State the preparation type.
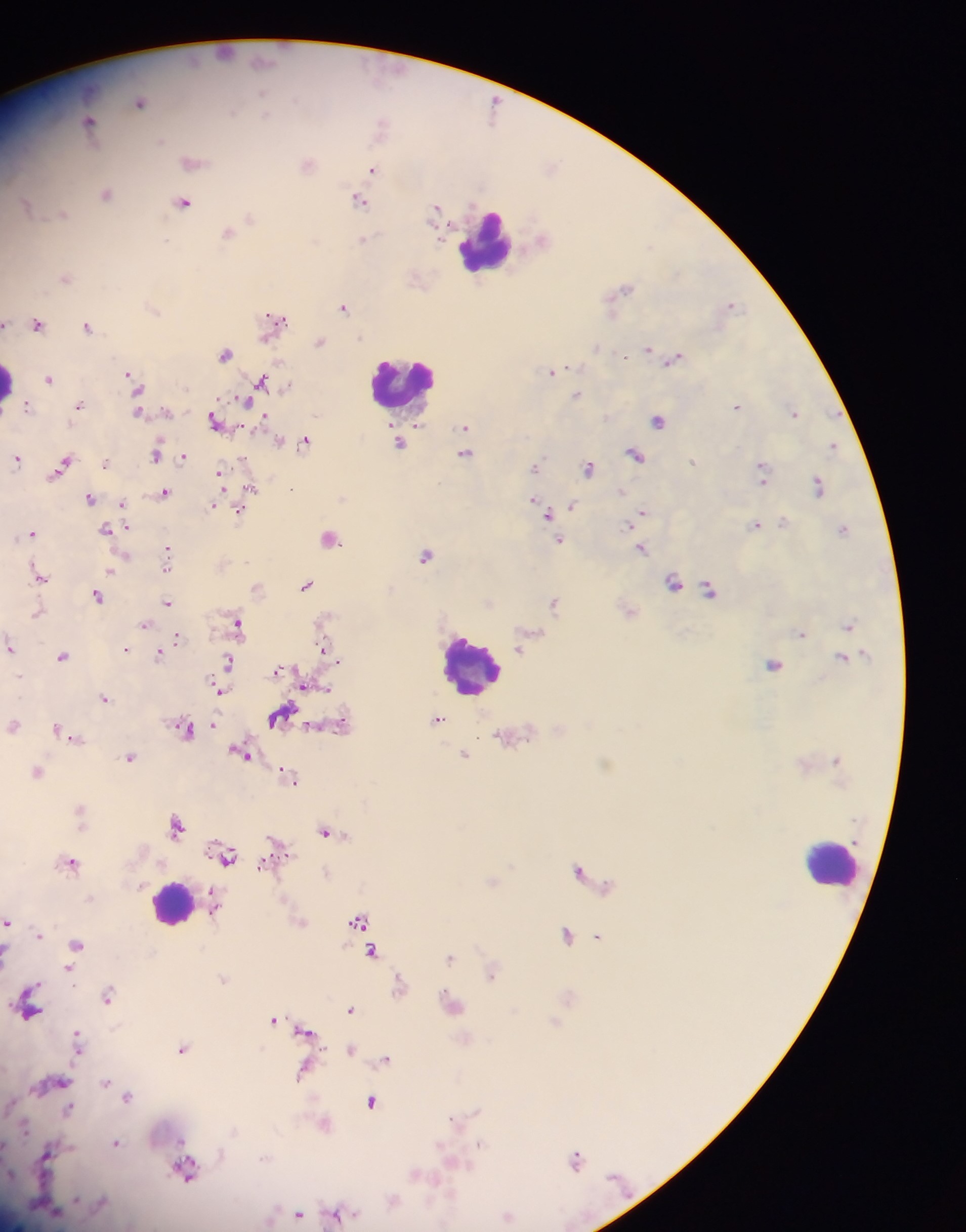

Thick blood film.

Approximate centers as {x, y} in pixels. Malaria parasite locations: {225, 52}, {141, 102}, {494, 107}, {90, 122}, {383, 125}, {192, 161}, {309, 163}, {373, 169}, {107, 192}, {359, 199}, {184, 201}, {27, 206}, {436, 209}, {62, 214}, {250, 218}, {229, 231}, {363, 240}, {66, 276}, {418, 278}, {625, 288}, {732, 303}, {344, 306}, {276, 319}, {38, 323}, {6, 324}, {88, 326}, {320, 341}, {597, 348}, {649, 348}, {226, 352}, {674, 359}, {553, 371}, {131, 374}, {50, 378}, {263, 381}, {138, 387}, {578, 395}, {244, 401}, {79, 405}, {27, 406}, {738, 406}, {139, 412}, {795, 412}, {265, 415}, {659, 420}, {217, 421}, {419, 426}, {465, 426}, {466, 438}, {306, 440}, {279, 441}, {401, 442}, {833, 446}, {158, 452}, {465, 453}, {636, 455}, {184, 456}, {18, 458}, {694, 461}, {106, 462}, {64, 463}, {536, 467}, {589, 467}, {764, 469}, {220, 475}, {820, 486}, {251, 487}, {293, 489}, {165, 492}, {91, 498}, {534, 499}, {123, 504}, {215, 504}, {572, 505}, {240, 510}, {643, 512}, {547, 514}, {784, 523}, {756, 525}, {126, 527}, {843, 529}, {108, 530}, {32, 533}, {331, 536}, {559, 539}, {642, 548}, {167, 552}, {426, 554}, {113, 570}, {39, 576}, {674, 581}, {308, 584}, {258, 588}, {710, 589}, {99, 595}, {554, 601}, {167, 602}, {630, 610}, {38, 613}, {238, 623}, {145, 624}, {849, 625}, {801, 633}, {177, 639}, {10, 647}, {171, 647}, {520, 648}, {126, 649}, {326, 651}, {160, 653}, {63, 656}, {844, 657}, {230, 661}, {774, 664}, {279, 670}, {307, 684}, {220, 690}, {104, 697}, {281, 715}, {438, 719}, {14, 724}, {214, 724}, {341, 724}, {185, 728}, {63, 731}, {513, 735}, {74, 736}, {242, 752}, {465, 754}, {130, 757}, {38, 771}, {289, 776}, {81, 811}, {178, 824}, {327, 831}, {278, 846}, {226, 855}, {72, 861}, {581, 871}, {326, 872}, {493, 880}, {214, 907}, {359, 920}, {8, 921}, {301, 921}, {568, 934}, {41, 935}, {599, 936}, {77, 944}, {373, 951}, {7, 952}, {450, 957}, {70, 969}, {493, 972}, {224, 979}, {400, 985}, {109, 994}, {569, 996}, {453, 1003}, {29, 1004}, {352, 1009}, {274, 1019}, {555, 1022}, {306, 1032}, {466, 1039}, {79, 1041}, {183, 1048}, {352, 1049}, {387, 1058}, {304, 1070}, {61, 1080}, {106, 1082}, {128, 1096}, {373, 1101}, {70, 1109}, {456, 1121}, {324, 1123}, {116, 1143}, {48, 1154}, {577, 1160}, {186, 1168}, {417, 1174}, {393, 1199}, {300, 1213}, {336, 1215}, {508, 1215}. Leukocyte locations: {486, 240}, {10, 380}, {402, 383}, {474, 664}, {833, 864}, {172, 903}. Sample from Ghana. Image is 966×1232 pixels. Photographed through a microscope with a mobile-phone camera. One field of view.